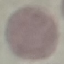

Malaria status: uninfected. Photographed with a smartphone camera at the microscope eyepiece. Cell patch, automatically extracted from a larger field of view and resized to 64 × 64 pixels. Giemsa-stained preparation. Thin blood film.